Locate leukocytes (white blood cells).
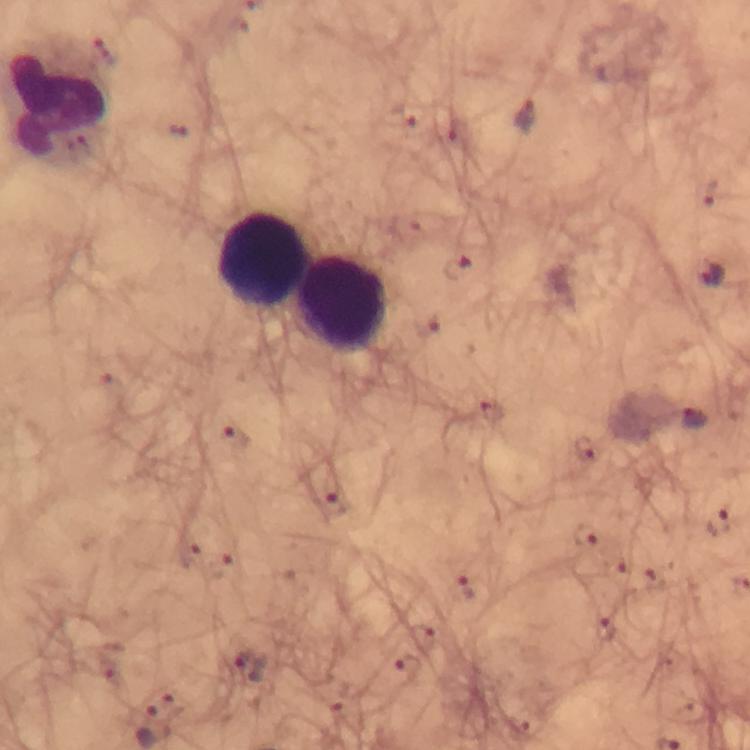
Approximate object centers, in pixels from the top-left corner.
Leukocytes: (x=259, y=259), (x=345, y=304).

preparation = thick smear
immersion oil = used
image size = 750×750 pixels
cropped from = one field of view
capture = smartphone camera through the microscope
malaria parasite locations = approximate object centers, in pixels from the top-left corner: (x=524, y=116), (x=459, y=271), (x=713, y=276), (x=489, y=413), (x=693, y=418), (x=235, y=438), (x=584, y=449), (x=335, y=505), (x=721, y=525), (x=583, y=535), (x=621, y=575), (x=463, y=589), (x=607, y=630), (x=251, y=667), (x=407, y=667)
context = from a diagnostic examination for malaria
stain = Giemsa
magnification = 100x